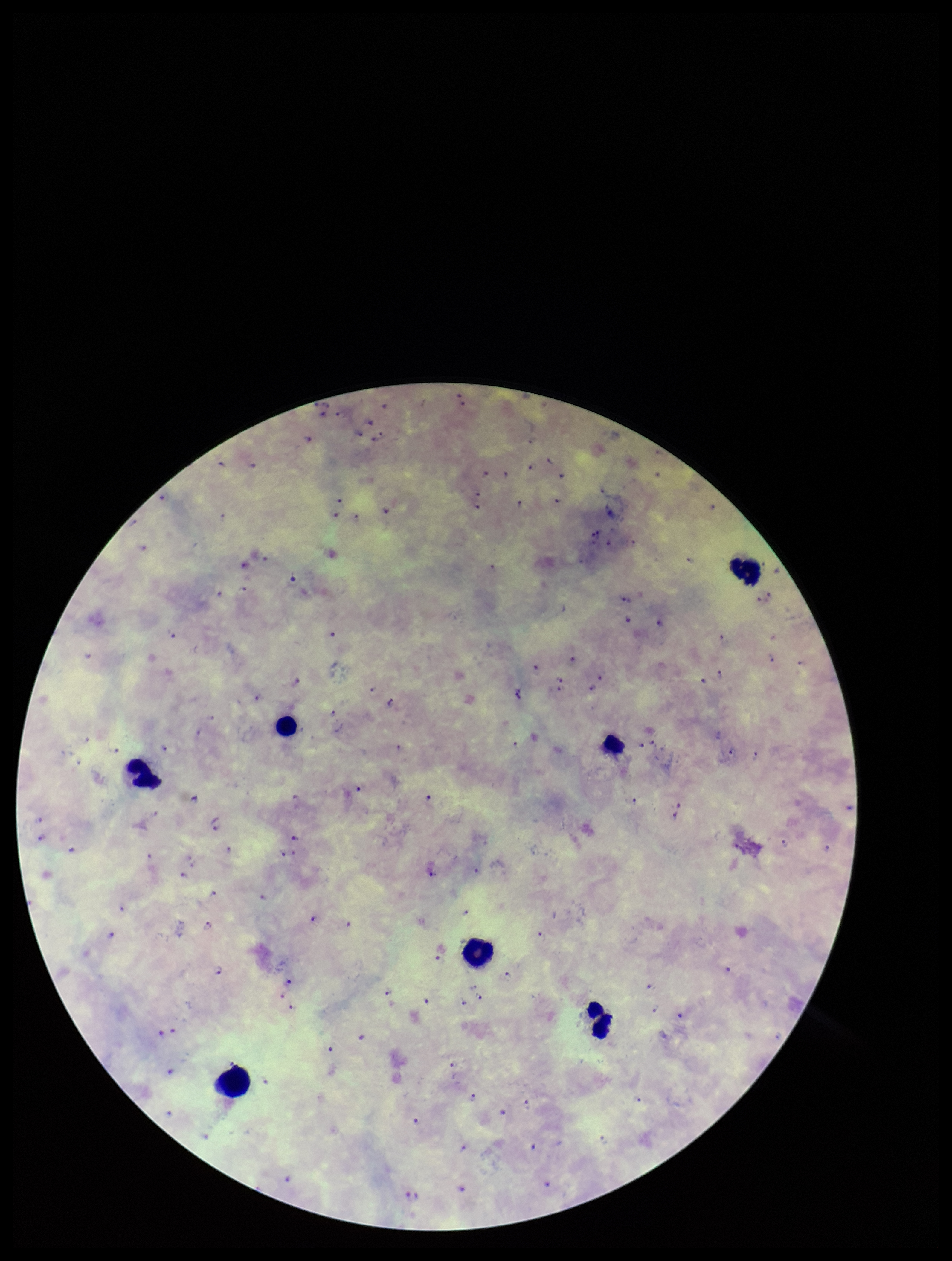
{
  "leukocyte_count": 7,
  "field_of_view": "one from this slide",
  "capture": "smartphone photograph through the microscope eyepiece",
  "preparation": "thick smear",
  "plasmodium_parasites": "seen",
  "stain": "Giemsa",
  "species_reported_for_this_patient": "Plasmodium falciparum",
  "image_size": "952×1261 pixels",
  "parasite_count": 83,
  "patient_malaria_status": "positive"
}